Assess this cell for malaria.
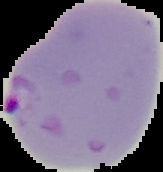
It is parasitized.

preparation: thin blood film
image_size: 163×172 pixels
image_type: segmented cell region with the area outside set to black